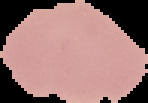
{
  "image_type": "segmented cell region on a black background",
  "image_size": "148×103 pixels",
  "result": "no malaria parasites seen",
  "preparation": "thin blood film"
}